Describe the morphology of the erythrocytes.
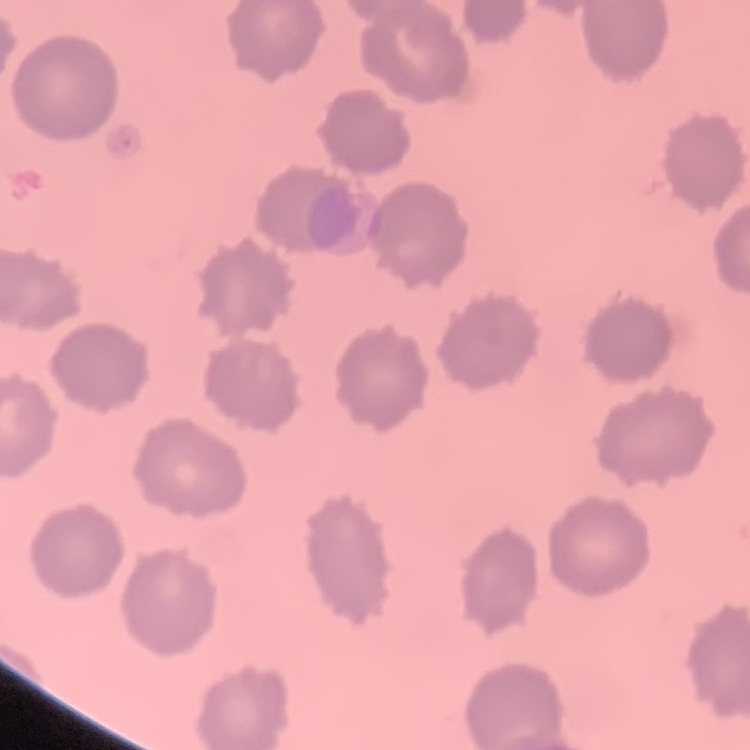

No rouleaux formation.

Summary:
  - Preparation: thin peripheral smear
  - Image type: square crop of a larger photomicrograph
  - Stain: Field's or Giemsa